Report the malaria status of this cell.
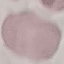

It is uninfected.

preparation = thin blood smear
capture = smartphone through the microscope eyepiece
stain = Giemsa
image type = automatically extracted cell patch, resized to 64 × 64 pixels